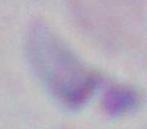 Toxoplasma gondii is shown. 1000x magnification. Photomicrograph.